Assess this cell for malaria.
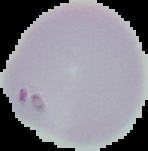
Parasitized.

Image is 148×151 pixels. Segmented cell region on a black background. From a thin blood smear.